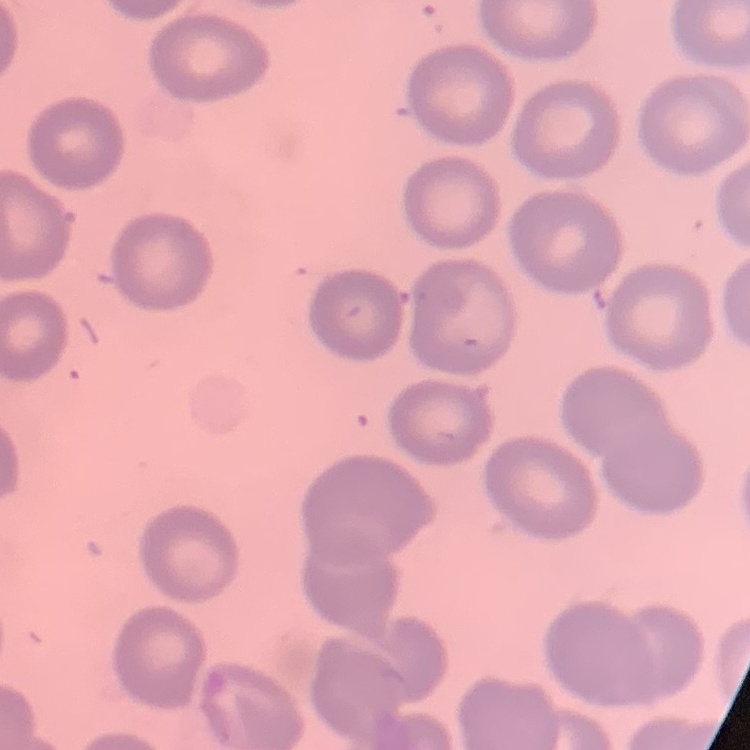 The erythrocytes exhibit no rouleaux formation. Field's or Giemsa stain. One tile cut from a larger photomicrograph. Thin blood smear.